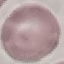
Malaria status: uninfected. Giemsa-stained preparation. Thin blood film. Automatically extracted cell patch, resized to 64 × 64 pixels. Photographed with a smartphone camera at the microscope eyepiece.